Identify the cell.
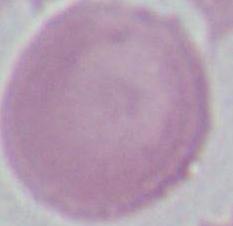
An erythrocyte.

Photomicrograph. 1000x magnification.